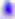

magnification = 400x
identification = Toxoplasma gondii
modality = photomicrograph